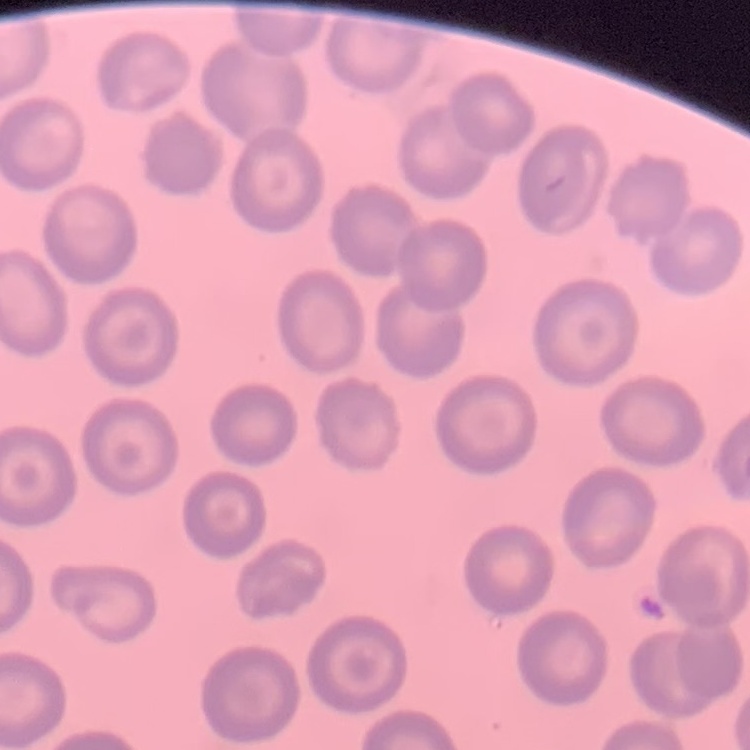
erythrocyte morphology = no rouleaux formation
preparation = thin blood smear
image type = one tile cut from a larger photomicrograph
stain = Field's or Giemsa